Assess for Plasmodium parasites.
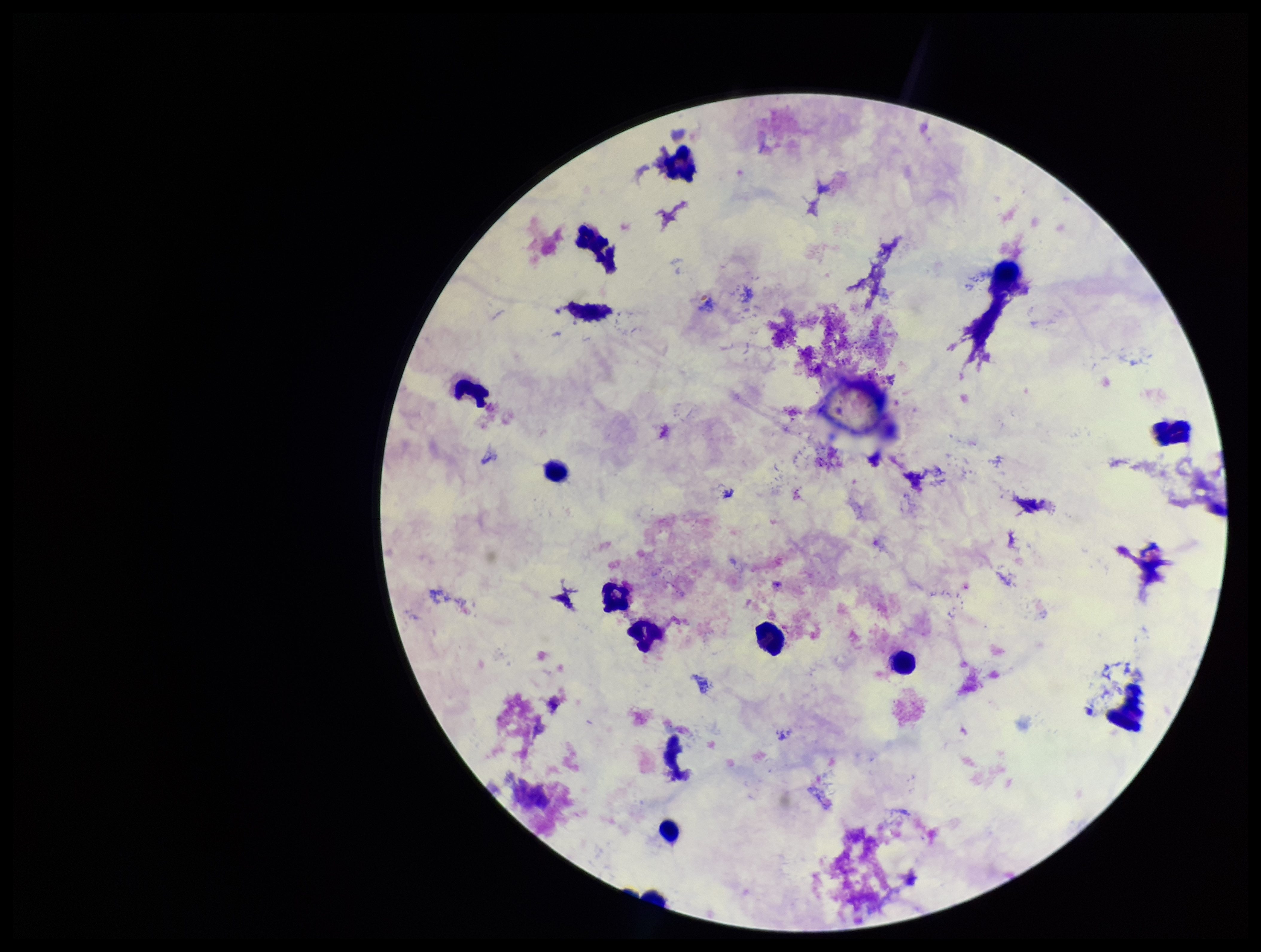

None identified.

Image is 1261×952 pixels. Preparation: thick smear. Giemsa stain. Photographed through the microscope eyepiece with a smartphone camera. Leukocyte count: 12. Patient malaria status: negative. Parasite count: 0. One field from this slide.